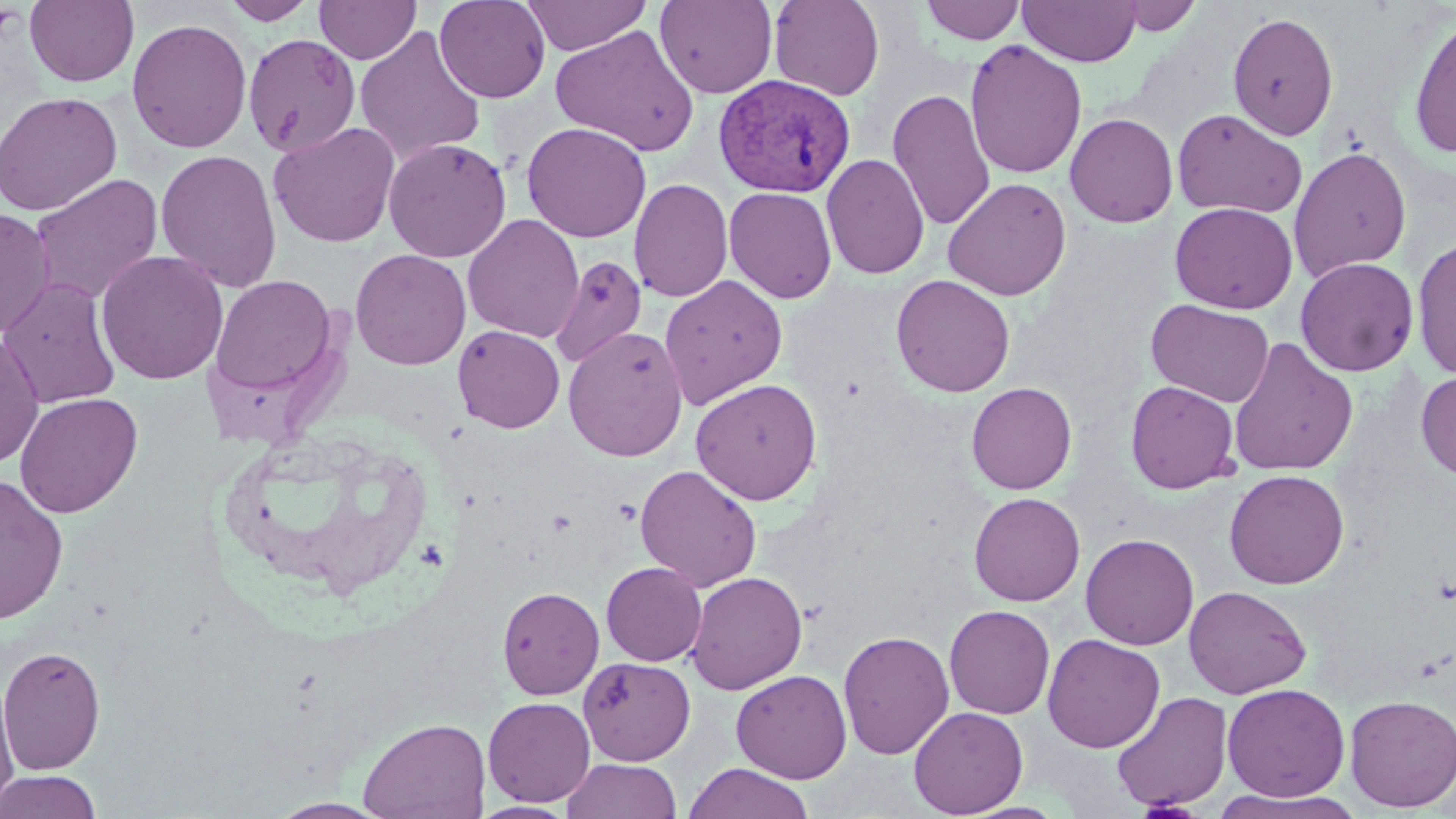
Approximate bounding boxes as (x1,y1)-(x2,y2) corner pairs in pixels. Uninfected red blood cell locations: (25,0)-(139,87), (222,0)-(319,25), (314,0)-(421,64), (434,0)-(551,103), (520,0)-(652,55), (654,0)-(778,99), (768,0)-(885,101), (920,1)-(1026,45), (1018,1)-(1141,66), (1112,1)-(1205,36), (1228,10)-(1339,141), (1407,14)-(1456,160), (126,17)-(252,154), (550,25)-(700,156), (354,26)-(487,166), (243,33)-(361,157), (964,39)-(1087,179), (888,88)-(997,230), (0,91)-(122,216), (1172,108)-(1308,219), (1064,113)-(1178,228), (268,121)-(401,248), (521,121)-(651,243), (383,137)-(511,262), (1288,145)-(1412,281), (155,149)-(282,294), (822,154)-(929,280), (30,174)-(164,306), (628,177)-(733,303), (943,177)-(1072,301), (723,186)-(837,303), (1170,202)-(1297,314), (0,207)-(56,339), (462,214)-(584,343), (1411,237)-(1456,381), (350,248)-(472,370), (95,250)-(229,385), (549,254)-(647,368), (1296,257)-(1419,376), (210,274)-(338,397), (658,274)-(788,409), (890,274)-(1015,397), (0,275)-(122,410), (1146,299)-(1274,407), (452,325)-(565,433), (562,326)-(688,462), (0,330)-(45,468), (1228,337)-(1359,476), (1415,370)-(1456,480), (691,377)-(822,505), (1125,380)-(1240,493), (966,381)-(1077,495), (14,392)-(143,518), (635,464)-(762,592), (1224,469)-(1350,590), (0,473)-(69,625), (968,491)-(1085,606), (1080,533)-(1199,650), (600,562)-(706,666), (685,570)-(807,694), (496,585)-(605,699), (1184,585)-(1312,699), (944,604)-(1055,719), (838,629)-(955,760), (1042,633)-(1165,753), (0,644)-(106,774), (577,657)-(695,766), (731,669)-(852,783), (0,679)-(19,810), (1222,682)-(1350,802), (1111,691)-(1233,812), (1344,694)-(1456,812), (483,696)-(596,806), (908,706)-(1029,817), (357,715)-(491,819), (560,758)-(683,819), (683,763)-(815,819), (0,770)-(102,819), (1208,789)-(1364,818), (268,798)-(391,818), (470,800)-(577,818). Platelet locations: (613,499)-(642,526), (546,509)-(577,536). Plasmodium vivax-infected red blood cell locations: (714,74)-(856,197). Slide-level diagnosis: Plasmodium vivax. Image is 1456×819 pixels. Thin blood film. Captured at 1000x magnification. One field of a larger specimen. Optical microscopy. May-Grünwald-Giemsa-stained preparation.